Comment on the morphology of the red blood cells.
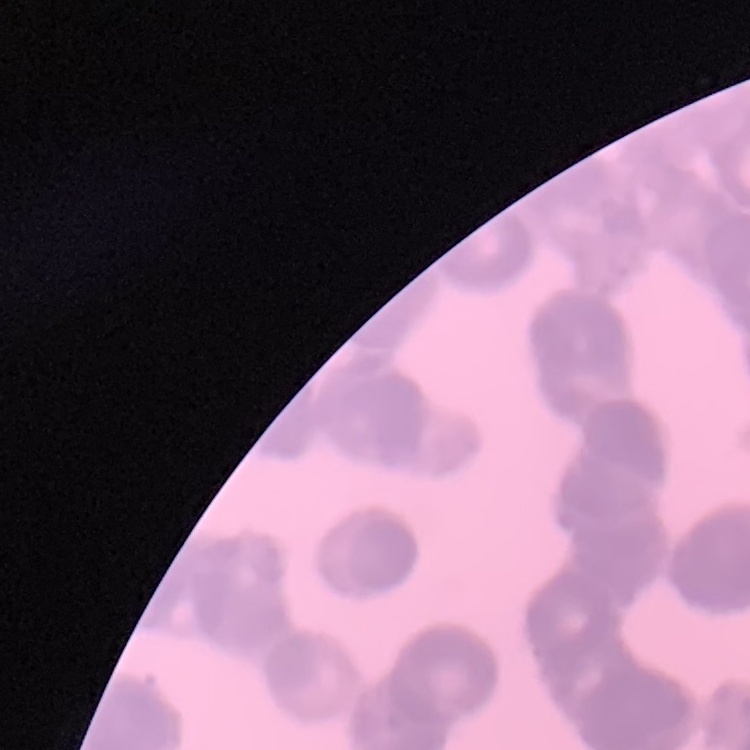
Rouleaux formation.

{
  "image_type": "one tile cut from a larger photomicrograph",
  "stain": "Field's or Giemsa",
  "preparation": "thin blood smear"
}